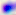

Summary:
  - Magnification: 400x
  - Identification: Toxoplasma gondii
  - Modality: photomicrograph